Assess this cell for malaria.
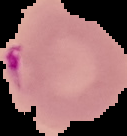

It is parasitized.

image size = 127×136 pixels
preparation = thin blood smear
image type = cell region segmented out of the field of view; surrounding area masked to black